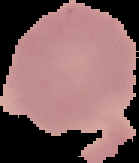

image size = 139×163 pixels
image type = segmented cell region with the area outside set to black
result = negative for malaria parasites
preparation = thin blood film